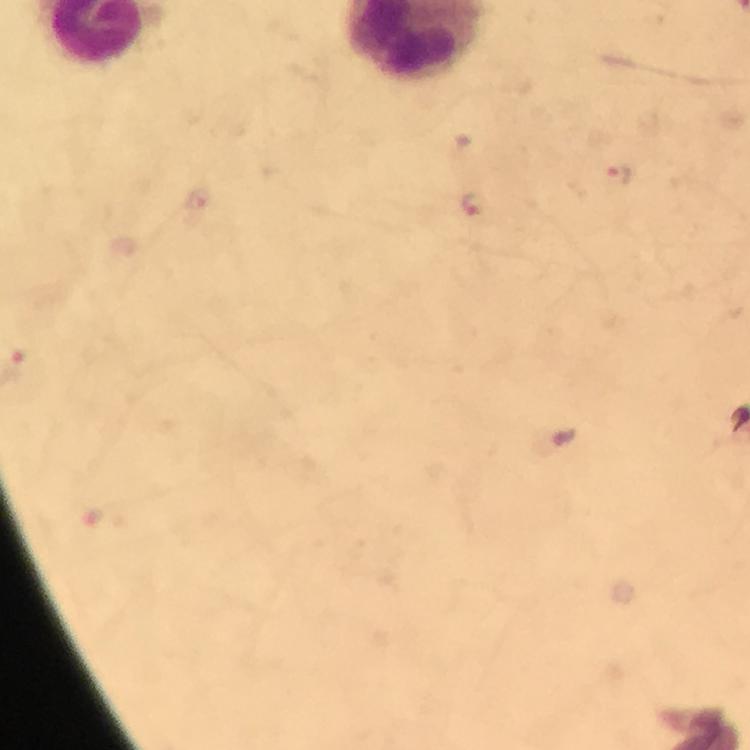

Approximate centers as [x, y] in pixels.
Summary:
  - Malaria parasite locations: [618, 177], [474, 203]
  - Cropped from: one field of view
  - Image size: 750×750 pixels
  - Magnification: 100x
  - Stain: Giemsa
  - Context: from a diagnostic examination for malaria
  - Preparation: thick blood film
  - Capture: smartphone camera through the microscope
  - Immersion oil: applied